State the blood parasite species.
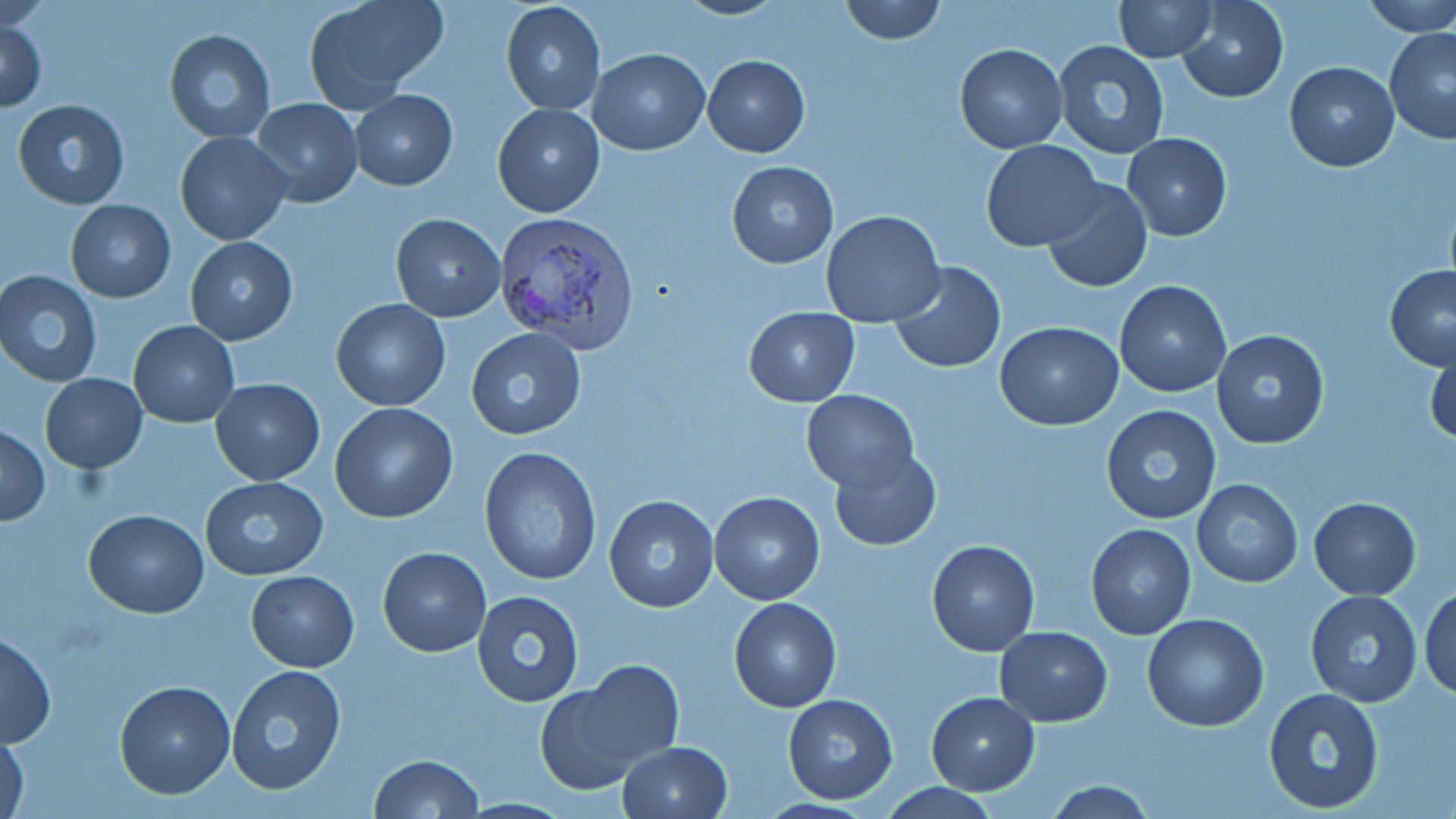

Plasmodium vivax.

Summary:
  - Coordinate format: approximate bounding boxes as (x1, y1, x2, y2) in pixels
  - Uninfected red blood cell locations: (304, 0, 447, 109), (499, 0, 605, 117), (674, 0, 786, 20), (838, 0, 947, 44), (1114, 0, 1217, 62), (1175, 0, 1289, 103), (1360, 0, 1456, 37), (0, 16, 48, 112), (1384, 27, 1456, 145), (164, 28, 276, 144), (1053, 39, 1170, 159), (954, 43, 1067, 153), (589, 49, 710, 155), (703, 54, 810, 157), (1284, 61, 1399, 171), (350, 90, 457, 190), (250, 97, 363, 206), (12, 99, 131, 209), (492, 103, 605, 217), (175, 131, 290, 245), (1122, 132, 1232, 240), (980, 140, 1102, 251), (726, 160, 839, 268), (1042, 178, 1152, 294), (66, 200, 176, 301), (821, 210, 945, 330), (390, 213, 506, 322), (185, 236, 297, 345), (890, 260, 1006, 374), (1384, 266, 1456, 370), (1, 270, 103, 386), (1115, 281, 1231, 399), (332, 298, 451, 411), (744, 305, 859, 407), (128, 320, 240, 428), (995, 321, 1124, 431), (465, 328, 588, 442), (1210, 329, 1329, 450), (1425, 335, 1456, 447), (40, 373, 146, 474), (209, 379, 324, 485), (801, 390, 920, 492), (330, 402, 459, 522), (1099, 404, 1222, 526), (1, 425, 48, 525), (478, 446, 603, 588), (828, 448, 943, 550), (199, 475, 328, 579), (1191, 480, 1303, 587), (709, 493, 825, 605), (603, 494, 721, 611), (1308, 496, 1422, 599), (83, 509, 210, 617), (1086, 524, 1196, 640), (927, 539, 1040, 656), (377, 547, 491, 657), (246, 570, 359, 672), (1418, 582, 1456, 699), (1306, 589, 1423, 707), (472, 591, 585, 707), (729, 597, 842, 712), (1142, 612, 1269, 731), (993, 627, 1113, 726), (1, 631, 56, 748), (574, 658, 685, 768), (224, 665, 346, 797), (534, 680, 647, 795), (115, 681, 236, 800), (1262, 685, 1384, 814), (925, 691, 1040, 794), (783, 694, 897, 805), (1, 729, 30, 819), (617, 740, 733, 819), (369, 754, 484, 818), (1044, 781, 1157, 817)
  - Plasmodium vivax-infected red blood cell locations: (496, 212, 642, 352)
  - Preparation: thin blood film
  - Modality: optical microscopy
  - Stain: May-Grünwald-Giemsa
  - Field of view: single
  - Magnification: 1000x
  - Image size: 1456×819 pixels